Name the blood parasite species.
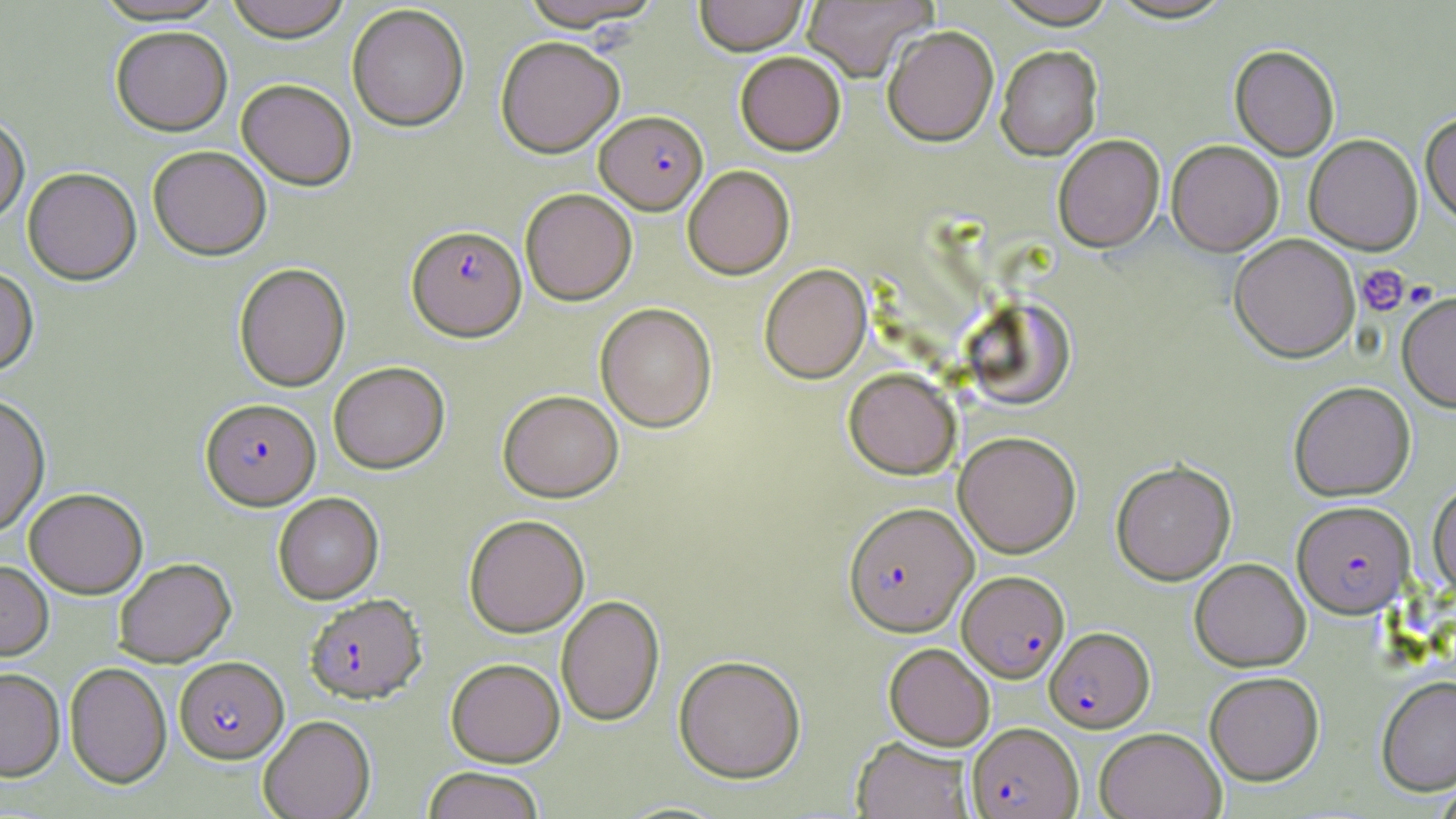

Plasmodium falciparum.

preparation = thin blood film
image size = 1456×819 pixels
uninfected red blood cell locations = approximate bounding boxes as [x1, y1, x2, y2] in pixels: [91, 0, 231, 26], [225, 0, 351, 42], [518, 0, 665, 33], [694, 0, 808, 56], [802, 0, 936, 83], [994, 0, 1118, 29], [1106, 0, 1236, 26], [347, 4, 470, 132], [111, 26, 233, 136], [883, 27, 999, 148], [495, 36, 625, 158], [996, 47, 1103, 162], [1229, 47, 1339, 161], [735, 51, 846, 156], [236, 79, 357, 190], [1420, 115, 1456, 228], [0, 116, 30, 227], [1305, 135, 1423, 256], [1053, 136, 1165, 253], [1167, 142, 1283, 257], [148, 146, 272, 260], [682, 165, 795, 280], [22, 167, 141, 285], [520, 188, 637, 306], [1229, 234, 1360, 363], [234, 263, 351, 392], [759, 264, 872, 384], [0, 266, 38, 378], [1397, 292, 1456, 413], [964, 297, 1076, 411], [595, 303, 717, 432], [328, 361, 450, 474], [844, 368, 961, 480], [1289, 382, 1416, 502], [498, 389, 623, 503], [0, 393, 51, 537], [953, 432, 1081, 558], [1111, 461, 1237, 585], [1427, 482, 1456, 599], [24, 488, 148, 599], [273, 492, 384, 604], [463, 514, 589, 638], [114, 558, 235, 667], [1189, 559, 1311, 672], [0, 561, 53, 661], [556, 595, 665, 727], [884, 643, 995, 750], [673, 655, 806, 783], [445, 658, 565, 767], [65, 662, 172, 788], [0, 668, 65, 781], [1205, 671, 1324, 785], [1376, 676, 1456, 795], [259, 714, 375, 819], [1094, 727, 1226, 819], [851, 737, 975, 819], [422, 767, 545, 819]
magnification = 1000x
stain = May-Grünwald-Giemsa
Plasmodium falciparum-infected red blood cell locations = approximate bounding boxes as [x1, y1, x2, y2] in pixels: [595, 111, 708, 214], [407, 225, 526, 341], [201, 398, 320, 509], [1291, 501, 1415, 619], [843, 502, 978, 637], [957, 570, 1069, 683], [304, 593, 426, 704], [1045, 626, 1154, 732], [175, 656, 289, 763], [966, 722, 1083, 819]
modality = optical microscopy
field of view = one of a larger specimen
platelet locations = approximate bounding boxes as [x1, y1, x2, y2] in pixels: [1356, 264, 1410, 317]